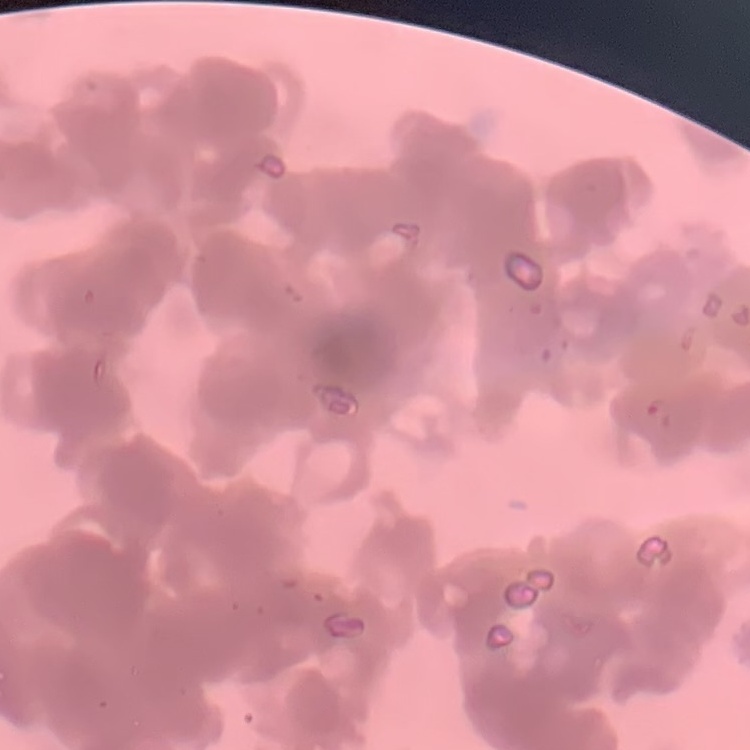

red blood cell morphology = rouleaux formation
stain = Field's or Giemsa
image type = one tile cut from a larger photomicrograph
preparation = thin peripheral smear